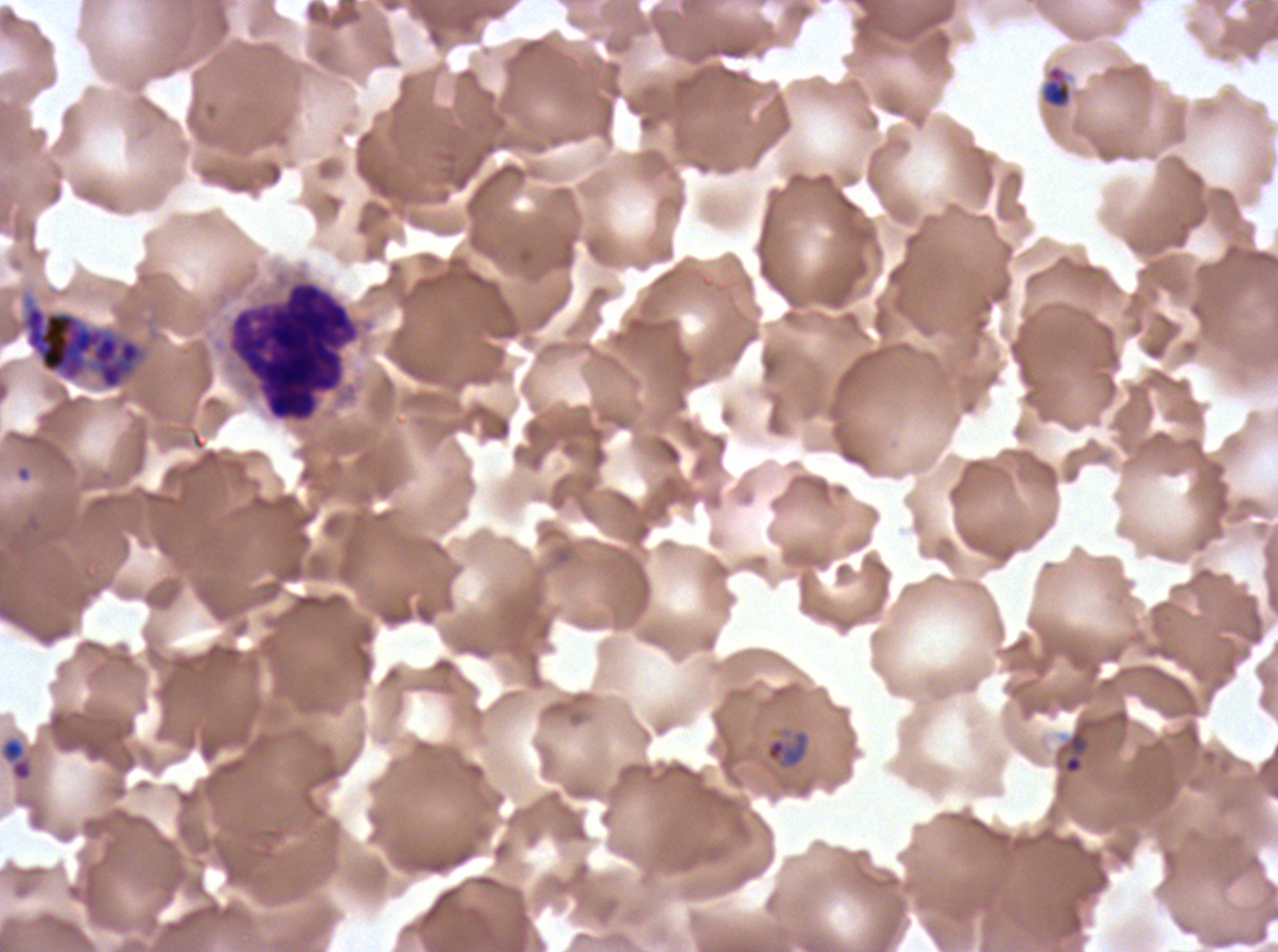
Approximate bounding boxes as (x1, y1, x2, y2) in pixels.
Summary:
  - Late-ring/early-trophozoite locations: (1039, 64, 1073, 110), (0, 737, 33, 782)
  - Ring locations: (1063, 729, 1088, 775), (766, 732, 808, 766)
  - Debris locations: (227, 280, 360, 422)
  - Late schizont locations: (21, 303, 144, 391)
  - Life-cycle stages observed: ring, late-ring/early-trophozoite, late schizont
  - Specimen: P. falciparum cultured ex vivo for 24 to 48 hours, from a patient in The Gambia
  - Image size: 1278×952 pixels
  - Field of view: one sub-image of a larger composite
  - Preparation: thin blood film
  - Stain: Giemsa